Assess this cell for malaria.
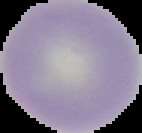

Uninfected.

Summary:
  - Image size: 142×133 pixels
  - Preparation: thin blood smear
  - Image type: cell region segmented out of the field of view; surrounding area masked to black